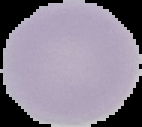

Image is 142×127 pixels. Segmented cell region on a black background. Malaria status: uninfected. From a thin blood smear.